Report the malaria status of this cell.
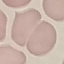
It is uninfected.

{
  "image_type": "cell patch, automatically extracted from a larger field of view and resized to 64 × 64 pixels",
  "capture": "smartphone camera at the microscope eyepiece",
  "preparation": "thin blood smear",
  "stain": "Giemsa"
}